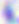
Summary:
  - Modality: photomicrograph
  - Magnification: 400x
  - Identification: Toxoplasma gondii